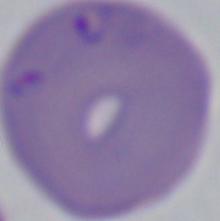
Summary:
  - Magnification: 1000x
  - Identification: Babesia
  - Modality: micrograph